Give the extent of all Plasmodium malariae-infected red blood cells.
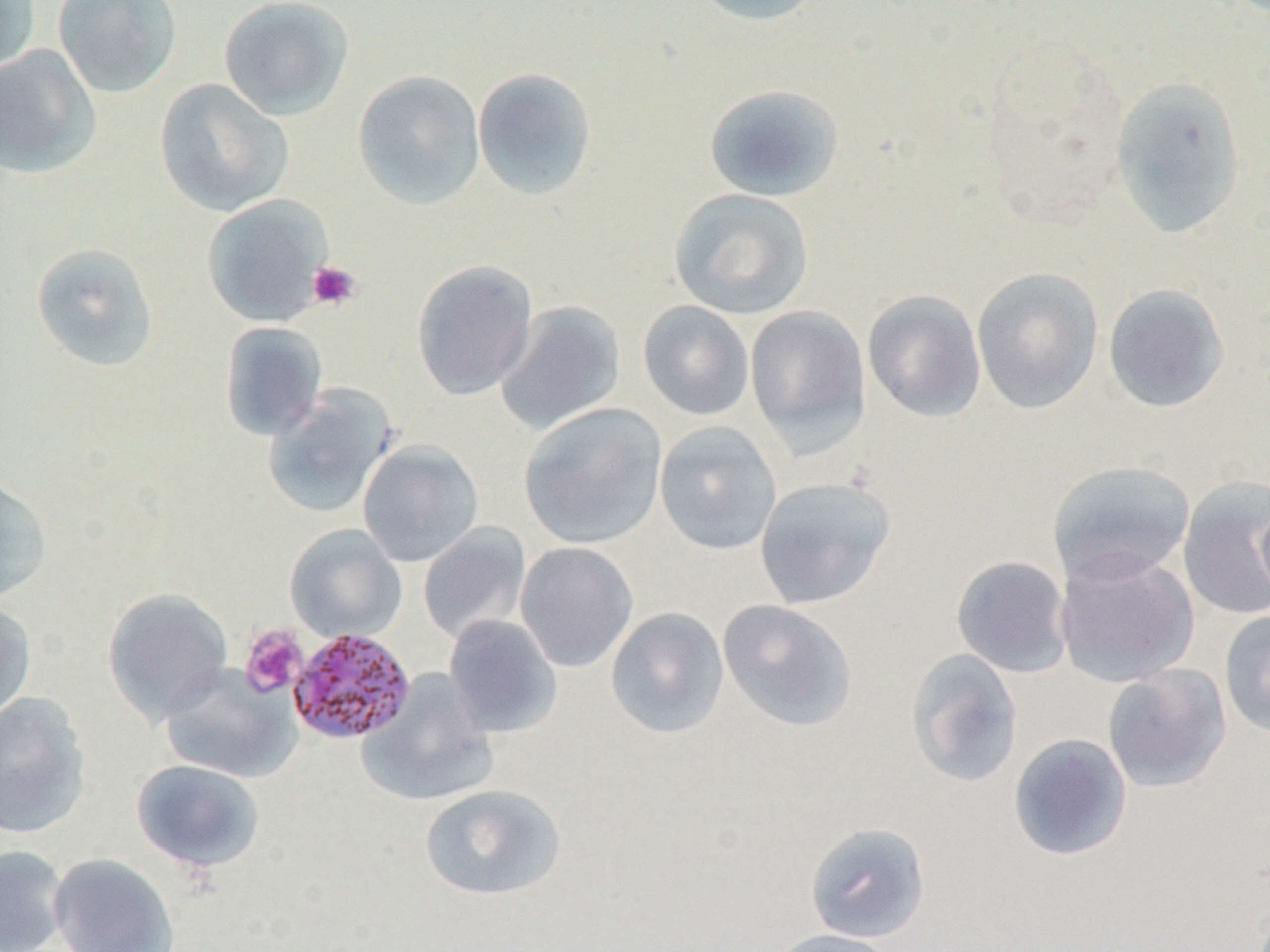
Approximate bounding boxes as (x1,y1)-(x2,y2) corner pairs in pixels.
Plasmodium malariae-infected red blood cells: (287,627)-(416,744).

slide-level diagnosis = Plasmodium malariae
field of view = one of a larger specimen
platelet locations = approximate bounding boxes as (x1,y1)-(x2,y2) corner pairs in pixels: (307,261)-(362,312), (239,626)-(307,697)
uninfected red blood cell locations = approximate bounding boxes as (x1,y1)-(x2,y2) corner pairs in pixels: (0,0)-(41,74), (53,0)-(183,99), (218,0)-(355,121), (689,0)-(824,26), (0,45)-(102,180), (472,67)-(598,201), (352,71)-(486,210), (1109,76)-(1248,239), (154,78)-(294,218), (702,84)-(846,203), (668,188)-(815,321), (202,194)-(334,327), (30,242)-(160,373), (411,260)-(538,401), (971,267)-(1104,415), (1102,283)-(1231,414), (862,290)-(987,423), (495,300)-(627,435), (638,300)-(755,421), (745,305)-(871,454), (219,321)-(329,441), (261,383)-(398,520), (519,402)-(668,550), (654,421)-(782,556), (358,440)-(484,567), (1047,460)-(1196,585), (0,474)-(53,604), (754,477)-(896,609), (1177,477)-(1270,621), (1256,497)-(1270,610), (284,524)-(407,642), (418,524)-(531,644), (516,542)-(638,672), (1055,547)-(1200,687), (951,554)-(1073,678), (101,588)-(234,725), (717,599)-(860,733), (0,601)-(37,720), (605,607)-(730,739), (1219,608)-(1270,739), (443,614)-(563,738), (906,649)-(1024,788), (159,663)-(301,783), (1101,663)-(1232,793), (357,670)-(499,807), (0,692)-(93,839), (1007,733)-(1133,862), (130,759)-(267,874), (418,783)-(567,902), (805,821)-(931,943), (0,845)-(70,952), (48,853)-(179,952), (766,928)-(903,952)
magnification = 1000x
preparation = thin blood smear
image size = 1270×952 pixels
modality = light microscopy